Give the position of every leukocyte visible.
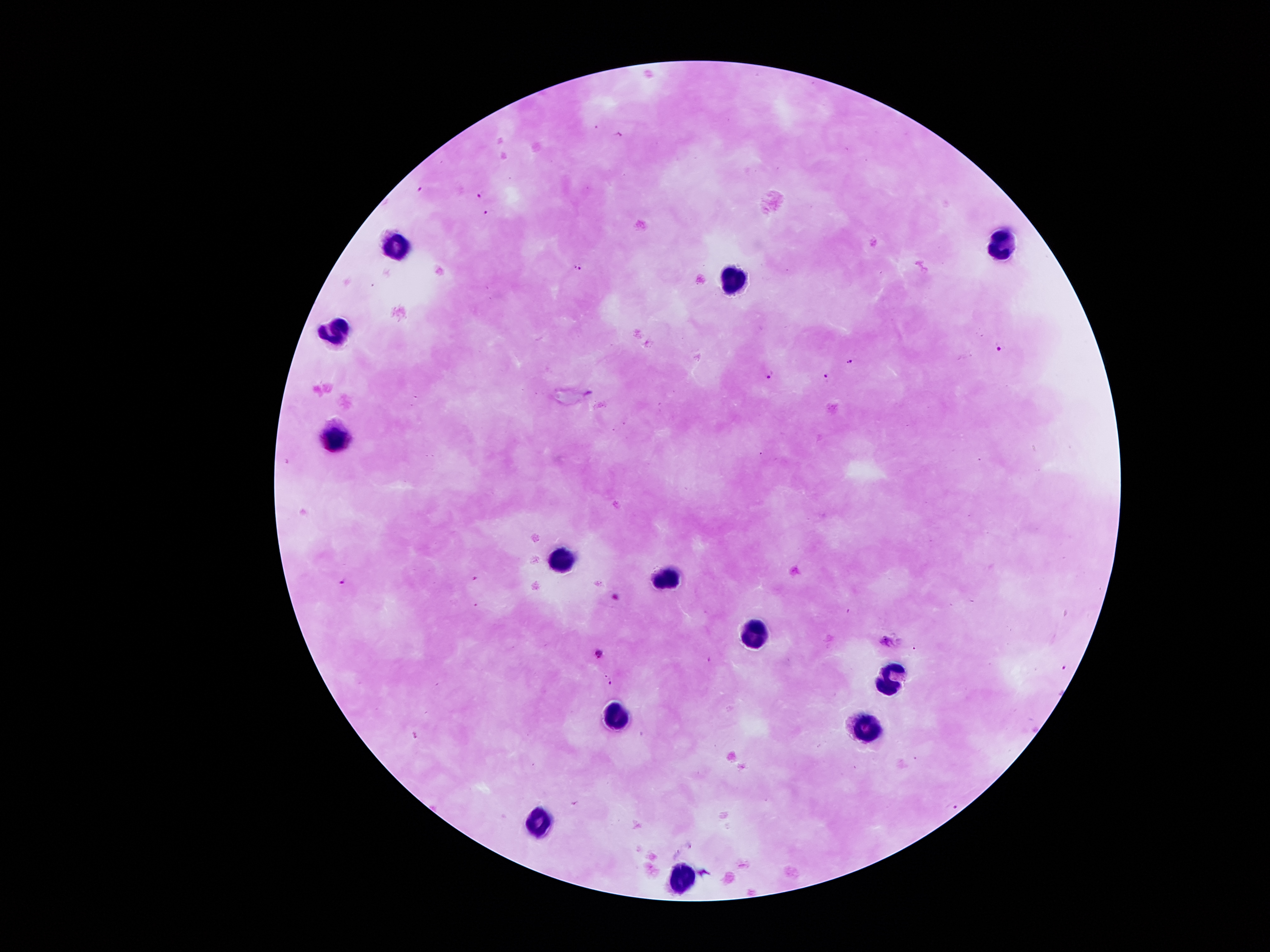

Approximate centers as {x, y} in pixels.
Leukocytes: {394, 244}, {1002, 249}, {738, 282}, {339, 324}, {332, 440}, {563, 560}, {665, 576}, {751, 633}, {890, 682}, {610, 717}, {864, 726}, {538, 822}, {682, 876}.

Plasmodium parasite locations: {422, 188}, {480, 195}, {488, 210}, {578, 266}, {1000, 347}, {849, 361}, {768, 373}, {827, 378}, {345, 578}, {887, 641}, {600, 653}, {610, 681}, {953, 805}. One field from this slide. 100x magnification. Thick peripheral-blood smear. Patient malaria status: infected with Plasmodium falciparum. Giemsa stain. Image is 1270×952 pixels. Smartphone photograph taken through the microscope eyepiece.